Report the malaria status of this cell.
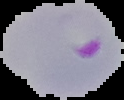

It is parasitized.

image size = 124×100 pixels
preparation = thin blood film
image type = segmented cell region with the area outside set to black